Classify this cell by malaria status.
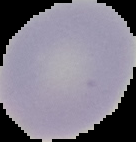
Uninfected.

Summary:
  - Preparation: thin blood smear
  - Image type: segmented cell region on a black background
  - Image size: 136×142 pixels